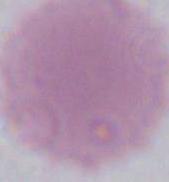

A red blood cell is seen. 1000x magnification. Micrograph.